Evaluate for malaria.
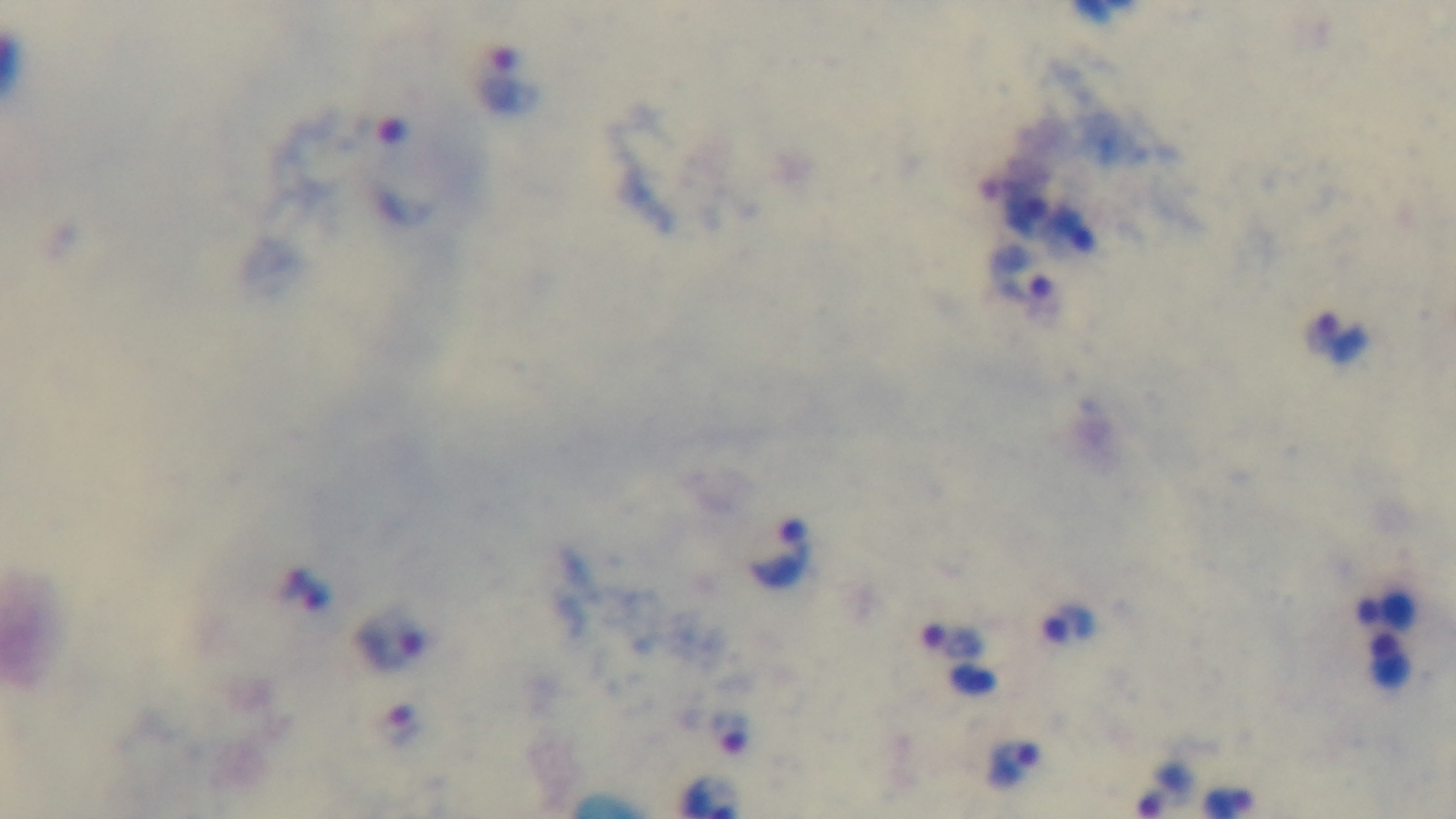
Infected.

Summary:
  - Preparation: thick
  - Capture: mounted 4K digital camera
  - Modality: light microscopy
  - Stain: Giemsa
  - Field of view: one from the slide
  - Objective: 100x oil immersion